Locate and identify every blood parasite.
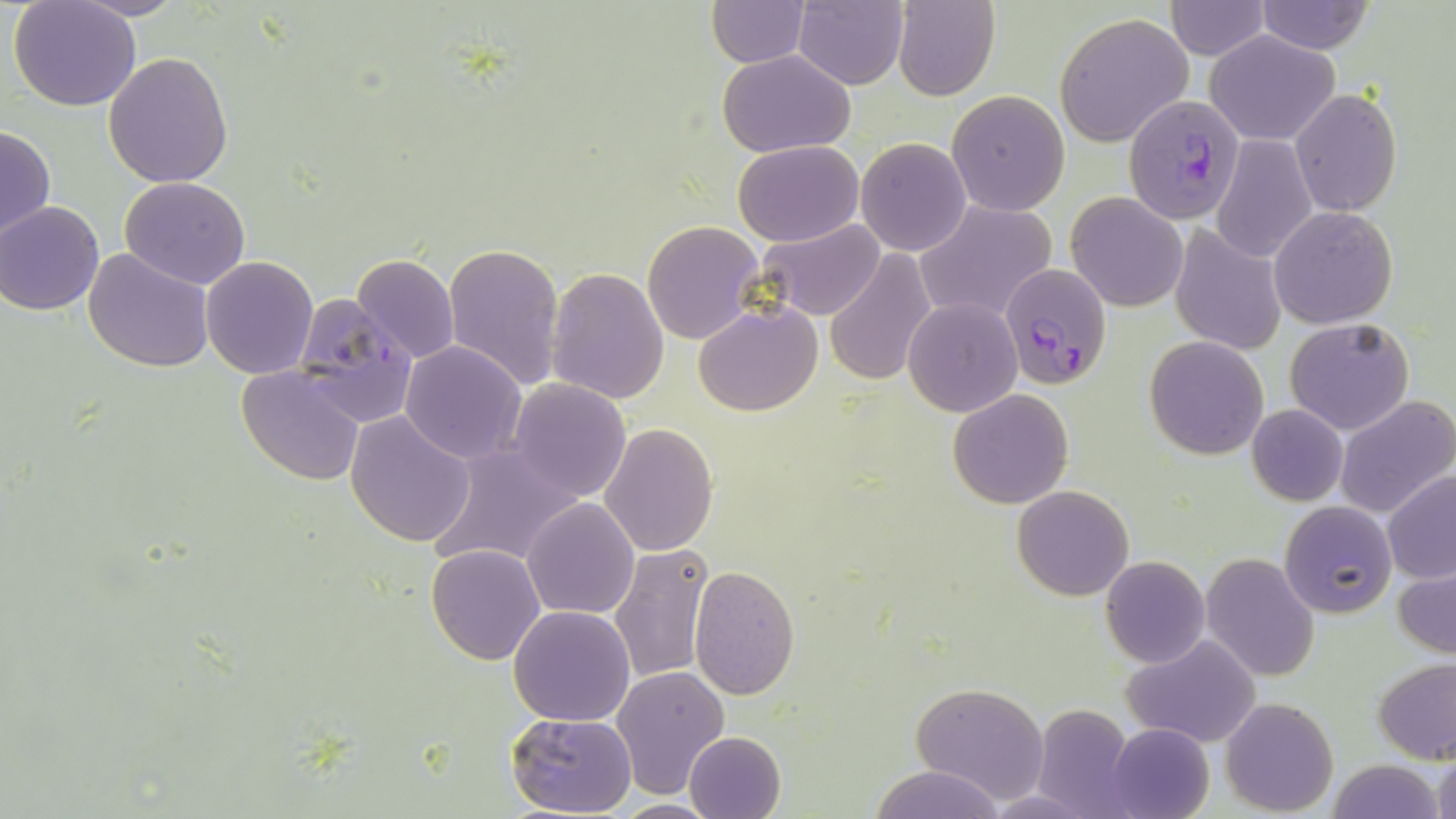
Approximate bounding boxes as named x1/y1/x2/y2 corners in pixels.
Plasmodium falciparum-infected red blood cells: (x1=1124, y1=94, x2=1244, y2=225), (x1=1000, y1=264, x2=1111, y2=394), (x1=292, y1=294, x2=419, y2=427).
No Plasmodium ovale, Plasmodium malariae, Plasmodium vivax, Babesia divergens, or Trypanosoma brucei observed.

Summary:
  - Uninfected red blood cell locations: (x1=893, y1=0, x2=999, y2=101), (x1=1164, y1=0, x2=1271, y2=59), (x1=9, y1=1, x2=142, y2=112), (x1=71, y1=1, x2=188, y2=20), (x1=1255, y1=1, x2=1375, y2=54), (x1=706, y1=2, x2=812, y2=68), (x1=794, y1=2, x2=909, y2=89), (x1=1053, y1=12, x2=1194, y2=148), (x1=1205, y1=31, x2=1341, y2=146), (x1=717, y1=50, x2=856, y2=157), (x1=102, y1=52, x2=234, y2=188), (x1=1290, y1=89, x2=1403, y2=216), (x1=947, y1=91, x2=1070, y2=216), (x1=0, y1=123, x2=55, y2=246), (x1=1212, y1=136, x2=1317, y2=263), (x1=857, y1=138, x2=971, y2=256), (x1=733, y1=139, x2=864, y2=246), (x1=120, y1=176, x2=251, y2=289), (x1=1068, y1=192, x2=1186, y2=312), (x1=916, y1=200, x2=1060, y2=322), (x1=0, y1=202, x2=104, y2=315), (x1=1270, y1=205, x2=1398, y2=328), (x1=753, y1=219, x2=884, y2=321), (x1=642, y1=220, x2=765, y2=345), (x1=1170, y1=226, x2=1287, y2=355), (x1=443, y1=242, x2=565, y2=393), (x1=84, y1=247, x2=214, y2=371), (x1=824, y1=249, x2=940, y2=387), (x1=351, y1=252, x2=461, y2=366), (x1=200, y1=256, x2=319, y2=378), (x1=547, y1=267, x2=671, y2=404), (x1=903, y1=298, x2=1022, y2=417), (x1=694, y1=303, x2=823, y2=417), (x1=1285, y1=317, x2=1414, y2=435), (x1=1144, y1=336, x2=1269, y2=458), (x1=399, y1=342, x2=527, y2=465), (x1=236, y1=365, x2=364, y2=484), (x1=506, y1=380, x2=632, y2=503), (x1=948, y1=388, x2=1074, y2=510), (x1=1333, y1=395, x2=1456, y2=518), (x1=1246, y1=404, x2=1347, y2=506), (x1=345, y1=410, x2=476, y2=547), (x1=600, y1=422, x2=718, y2=556), (x1=427, y1=442, x2=583, y2=571), (x1=1382, y1=471, x2=1456, y2=586), (x1=1012, y1=485, x2=1132, y2=600), (x1=521, y1=497, x2=639, y2=619), (x1=1280, y1=502, x2=1396, y2=619), (x1=425, y1=544, x2=545, y2=665), (x1=609, y1=544, x2=713, y2=685), (x1=1200, y1=552, x2=1321, y2=683), (x1=1101, y1=555, x2=1210, y2=668), (x1=1392, y1=556, x2=1456, y2=663), (x1=690, y1=565, x2=800, y2=699), (x1=509, y1=605, x2=636, y2=727), (x1=1123, y1=634, x2=1262, y2=749), (x1=1373, y1=657, x2=1456, y2=764), (x1=610, y1=665, x2=729, y2=798), (x1=911, y1=681, x2=1052, y2=804), (x1=1221, y1=698, x2=1337, y2=816), (x1=1030, y1=702, x2=1142, y2=815), (x1=506, y1=712, x2=638, y2=817), (x1=1107, y1=722, x2=1214, y2=819), (x1=683, y1=731, x2=786, y2=819), (x1=1430, y1=746, x2=1455, y2=819), (x1=1328, y1=758, x2=1444, y2=819), (x1=868, y1=764, x2=1006, y2=819), (x1=608, y1=798, x2=726, y2=817)
  - Slide-level diagnosis: Plasmodium falciparum
  - Modality: light microscopy
  - Field of view: single
  - Preparation: thin blood film
  - Magnification: 1000x
  - Stain: May-Grünwald-Giemsa
  - Image size: 1456×819 pixels